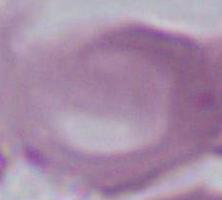
Summary:
  - Magnification: 1000x
  - Modality: photomicrograph
  - Identification: red blood cell